State which parasite is depicted.
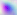

Toxoplasma gondii.

Summary:
  - Modality: micrograph
  - Magnification: 400x